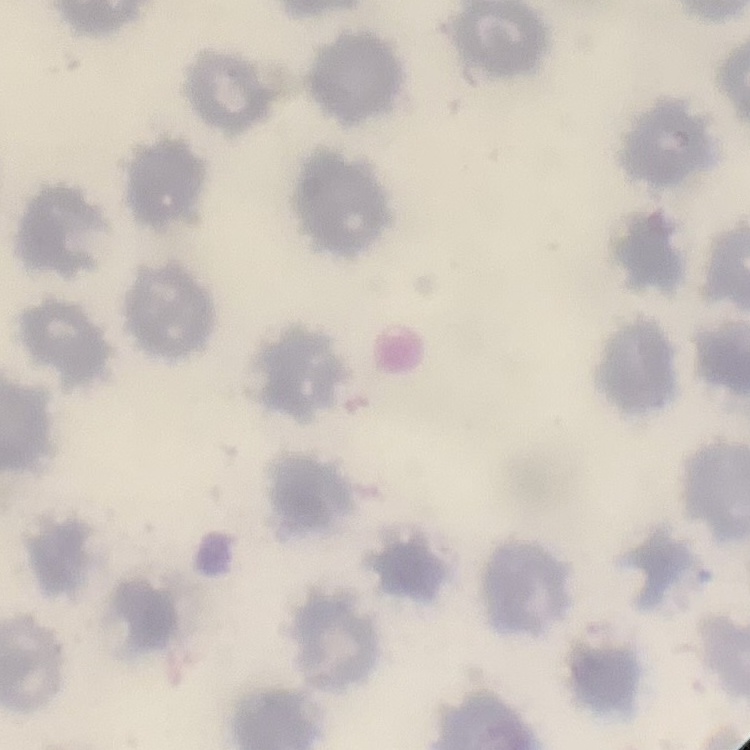

The red blood cells show no rouleaux formation. Thin blood film. One tile cut from a larger photomicrograph. Stained with either Field's or Giemsa.